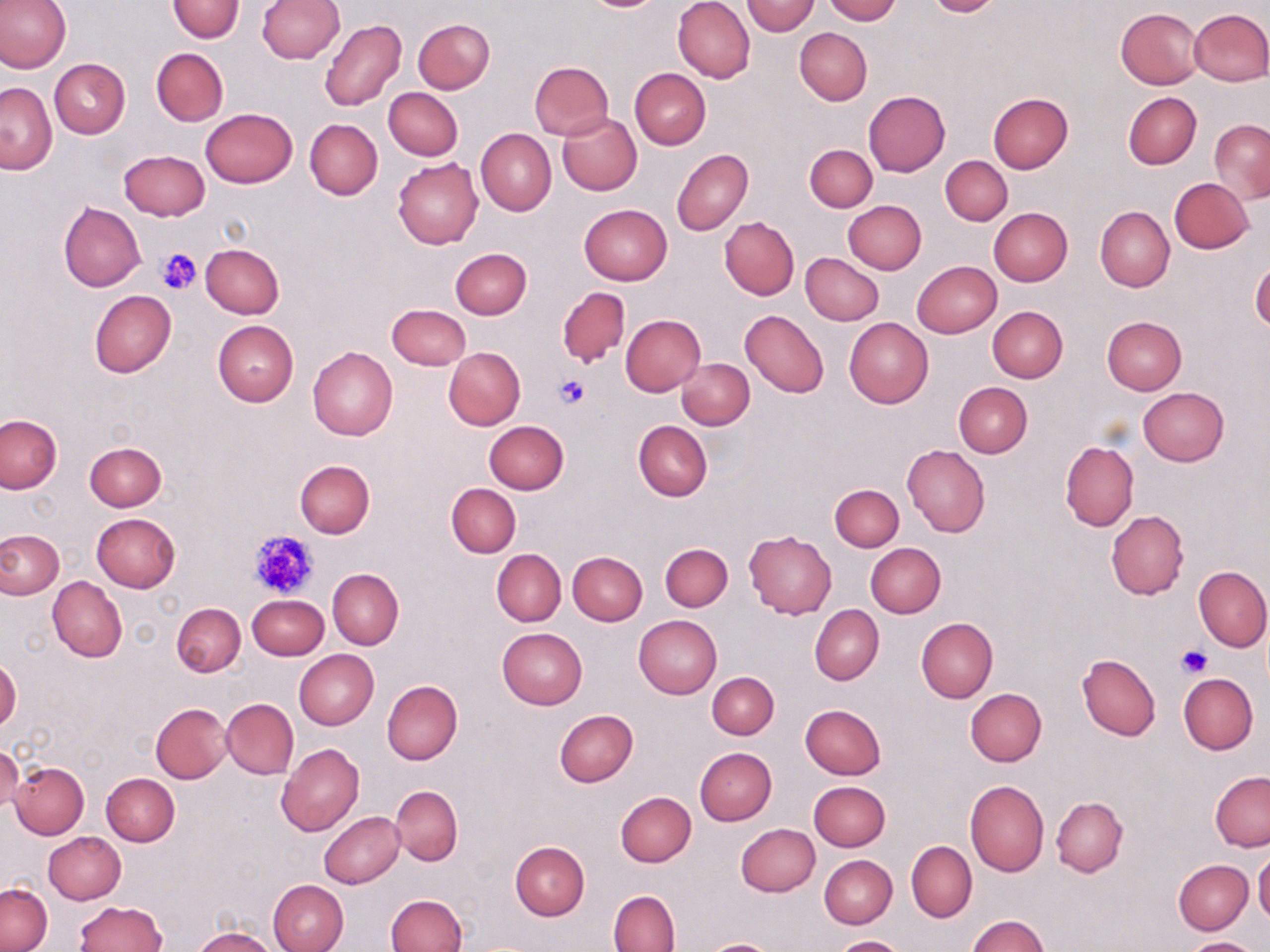

{
  "slide_level_diagnosis": "negative for blood parasites",
  "uninfected_red_blood_cell_locations": "approximate bounding boxes as (x1, y1, x2, y2) in pixels: (0, 0, 70, 74), (168, 0, 244, 44), (259, 0, 345, 63), (673, 0, 756, 83), (823, 0, 899, 24), (923, 0, 1003, 17), (742, 1, 819, 36), (1116, 7, 1203, 89), (1189, 8, 1270, 86), (413, 18, 495, 94), (319, 19, 407, 110), (795, 28, 871, 106), (151, 48, 227, 126), (50, 59, 130, 139), (529, 61, 615, 140), (630, 68, 710, 149), (0, 82, 56, 174), (384, 87, 462, 160), (862, 90, 951, 177), (1123, 92, 1202, 168), (988, 93, 1072, 174), (200, 108, 298, 188), (557, 112, 641, 196), (305, 118, 382, 200), (1209, 120, 1270, 203), (476, 128, 557, 216), (805, 145, 877, 212), (672, 149, 753, 235), (119, 150, 210, 221), (940, 155, 1012, 226), (393, 158, 484, 250), (1169, 177, 1253, 254), (843, 200, 926, 274), (58, 202, 146, 291), (578, 204, 673, 286), (1095, 206, 1175, 292), (989, 208, 1072, 286), (719, 216, 798, 300), (201, 244, 284, 318), (451, 247, 532, 319), (801, 253, 885, 325), (912, 260, 1001, 338), (1250, 262, 1270, 332), (557, 287, 630, 368), (89, 289, 175, 377), (386, 304, 471, 371), (987, 306, 1067, 383), (740, 309, 829, 399), (621, 314, 706, 396), (1102, 316, 1187, 395), (844, 317, 933, 407), (213, 321, 298, 405), (308, 346, 398, 440), (443, 347, 525, 429), (678, 358, 754, 430), (954, 382, 1032, 457), (1138, 387, 1228, 466), (0, 414, 63, 494), (634, 420, 712, 502), (484, 421, 569, 494), (1060, 441, 1139, 531), (84, 442, 165, 511), (902, 444, 989, 538), (294, 460, 375, 538), (447, 483, 521, 557), (830, 484, 904, 551), (1106, 509, 1188, 599), (91, 513, 181, 592), (1, 529, 64, 599), (743, 531, 837, 618), (660, 543, 733, 612), (866, 543, 945, 618), (492, 549, 566, 626), (568, 552, 647, 626), (1193, 565, 1270, 652), (328, 568, 404, 650), (47, 576, 127, 663), (248, 594, 329, 659), (172, 603, 246, 676), (810, 605, 884, 685), (634, 615, 722, 698), (916, 618, 997, 702), (497, 628, 586, 710), (295, 650, 378, 729), (1077, 653, 1160, 741), (1, 655, 21, 734), (707, 672, 779, 739), (1178, 673, 1257, 754), (382, 681, 463, 764), (964, 688, 1046, 766), (221, 698, 298, 779), (151, 703, 232, 782), (800, 704, 887, 779), (554, 709, 638, 787), (276, 743, 365, 836), (0, 745, 22, 813), (694, 747, 777, 825), (10, 761, 89, 838), (101, 772, 179, 846), (1210, 773, 1270, 851), (964, 780, 1049, 878), (808, 781, 890, 851), (390, 785, 463, 865), (615, 791, 695, 867), (1051, 797, 1127, 876), (319, 811, 404, 888), (736, 823, 820, 897), (44, 832, 125, 904), (510, 841, 589, 920), (905, 841, 977, 922), (1254, 850, 1270, 927), (819, 855, 896, 928), (1173, 859, 1253, 934), (267, 879, 349, 952), (1, 882, 52, 951), (608, 890, 680, 952), (385, 894, 465, 952), (75, 901, 167, 951), (971, 915, 1049, 952), (193, 928, 276, 951), (833, 935, 907, 952), (1184, 938, 1259, 952), (706, 940, 777, 952)",
  "image_size": "1270×952 pixels",
  "modality": "optical microscopy",
  "magnification": "1000x",
  "field_of_view": "one of a larger specimen",
  "stain": "May-Grünwald-Giemsa",
  "preparation": "thin blood smear",
  "platelet_locations": "approximate bounding boxes as (x1, y1, x2, y2) in pixels: (156, 249, 200, 295), (552, 373, 590, 410), (249, 530, 317, 598), (1175, 645, 1211, 679)"
}